Comment on the morphology of the red blood cells.
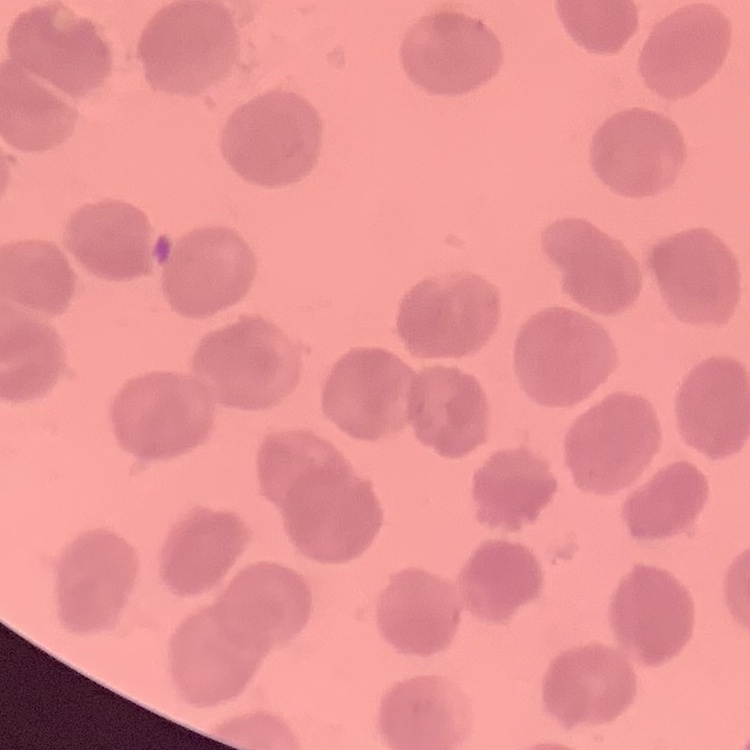

No rouleaux formation.

One tile cut from a larger photomicrograph. Field's or Giemsa stain. Thin peripheral smear.